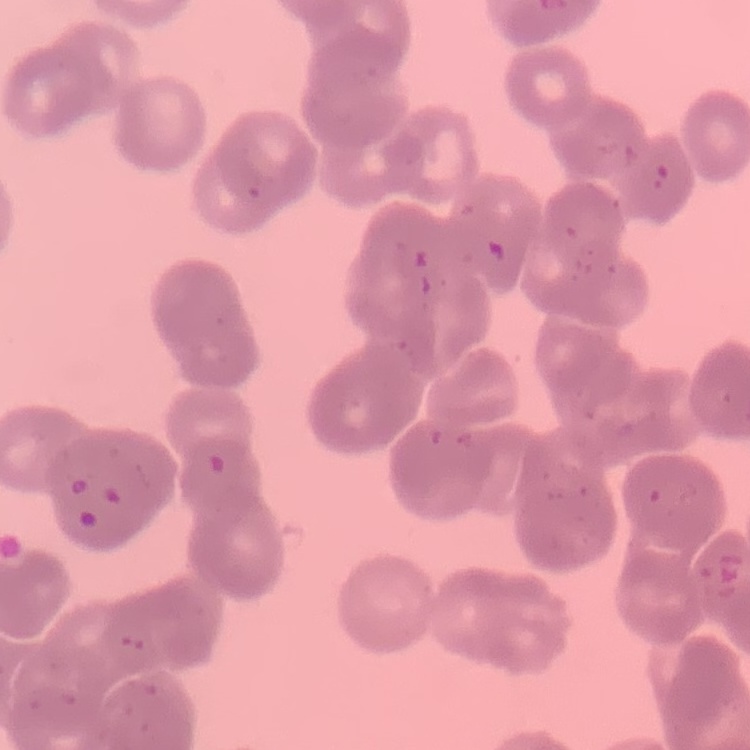

Summary:
  - Red blood cell morphology: rouleaux formation
  - Preparation: thin blood film
  - Image type: one tile cut from a larger photomicrograph
  - Stain: Field's or Giemsa